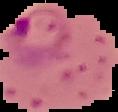
malaria status = parasitized
image type = segmented cell region with the area outside set to black
preparation = thin blood film
image size = 118×112 pixels